Describe the morphology of the erythrocytes.
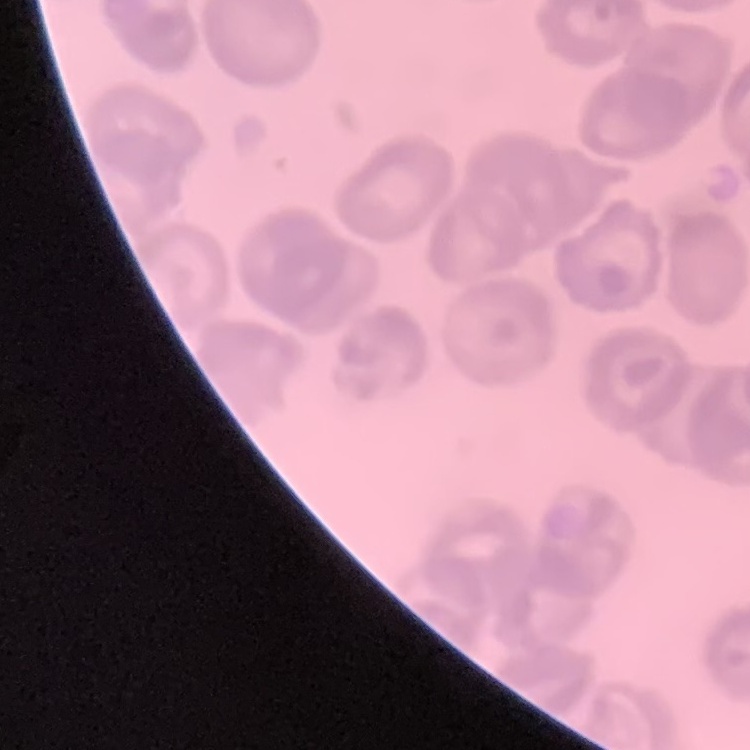

They show no rouleaux formation.

Field's or Giemsa stain. One tile cut from a larger photomicrograph. Thin blood film.